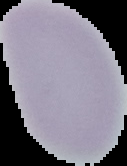

From a thin blood smear. Cell region segmented out of the field of view; the surrounding area is masked to black. Malaria status: uninfected. Image is 127×166 pixels.